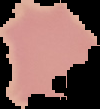

{
  "image_size": "100×109 pixels",
  "preparation": "thin blood film",
  "result": "no malaria parasites detected",
  "image_type": "segmented cell region on a black background"
}